Describe the morphology of the erythrocytes.
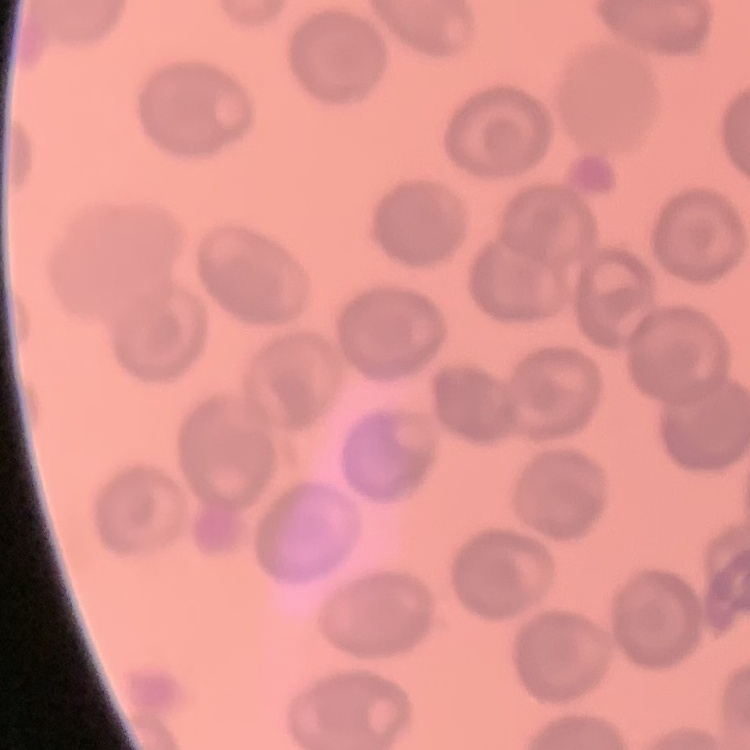

They show no rouleaux formation.

image type = one tile cut from a larger photomicrograph
stain = Field's or Giemsa
preparation = thin peripheral smear